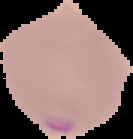
Summary:
  - Image size: 133×139 pixels
  - Preparation: thin blood smear
  - Result: malaria parasites identified
  - Image type: segmented cell region on a black background